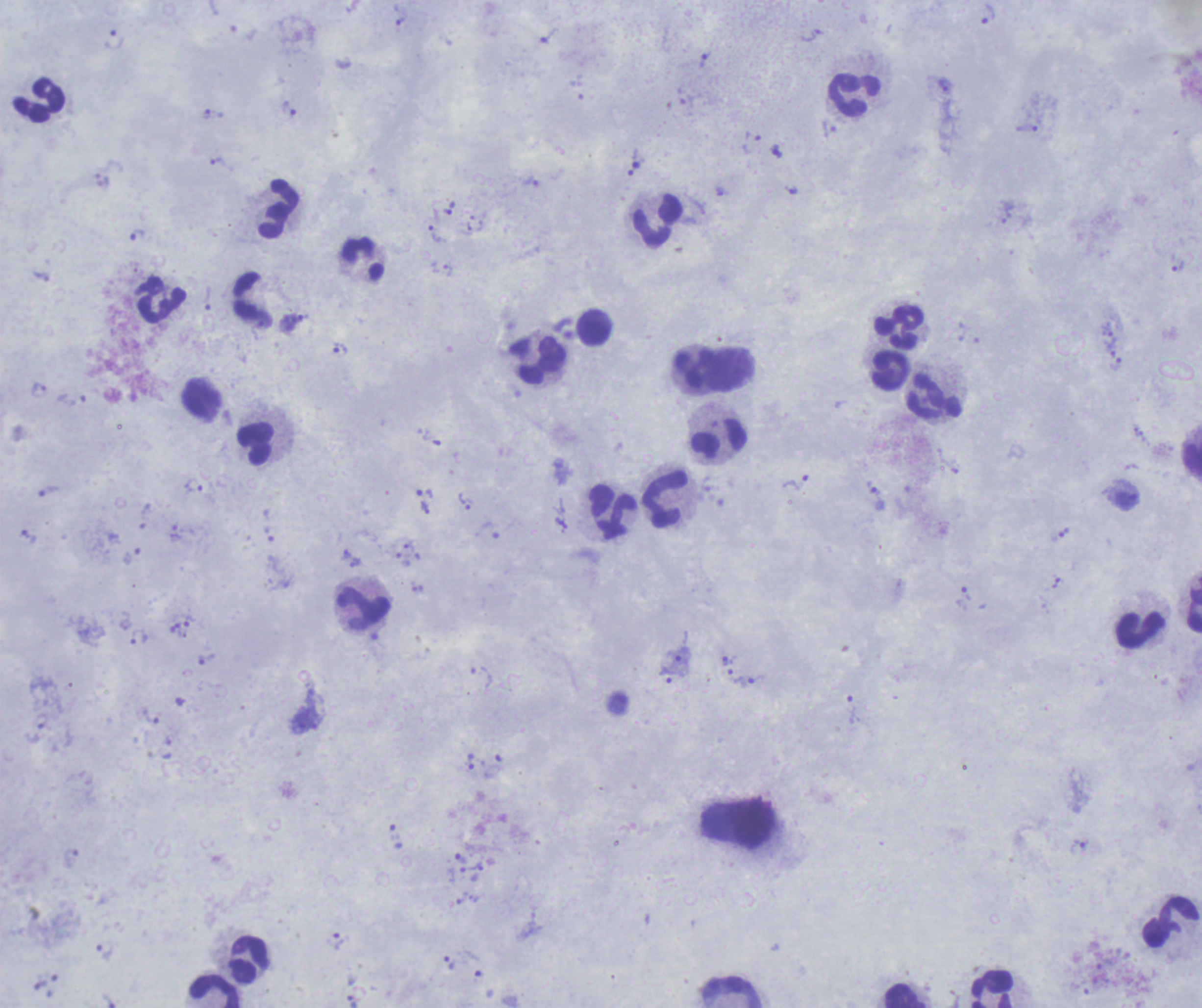 One field from this slide. Romanowsky stain. Thick blood film. Image is 1202×1008 pixels.